Assess this cell for malaria.
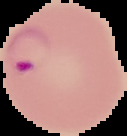
Parasitized.

The area outside the segmented cell region is set to black. From a thin blood film. Image is 127×136 pixels.